Name the cell type shown.
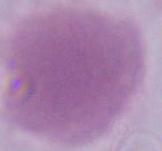
An erythrocyte.

magnification = 1000x
modality = micrograph